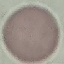 Result: no malaria parasites detected. Thin smear of blood. Giemsa-stained preparation. Photographed with a smartphone camera at the microscope eyepiece. Automatically extracted cell patch, resized to 64 × 64 pixels.